Report the malaria status of this cell.
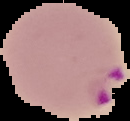
Parasitized.

Summary:
  - Image type: cell region segmented out of the field of view; surrounding area masked to black
  - Image size: 130×121 pixels
  - Preparation: thin blood smear